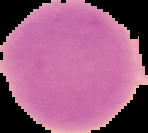
preparation: thin blood smear
image_size: 148×133 pixels
malaria_status: uninfected
image_type: cell region segmented out of the field of view; surrounding area masked to black